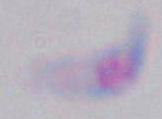

Toxoplasma gondii is seen. Photomicrograph. 1000x magnification.